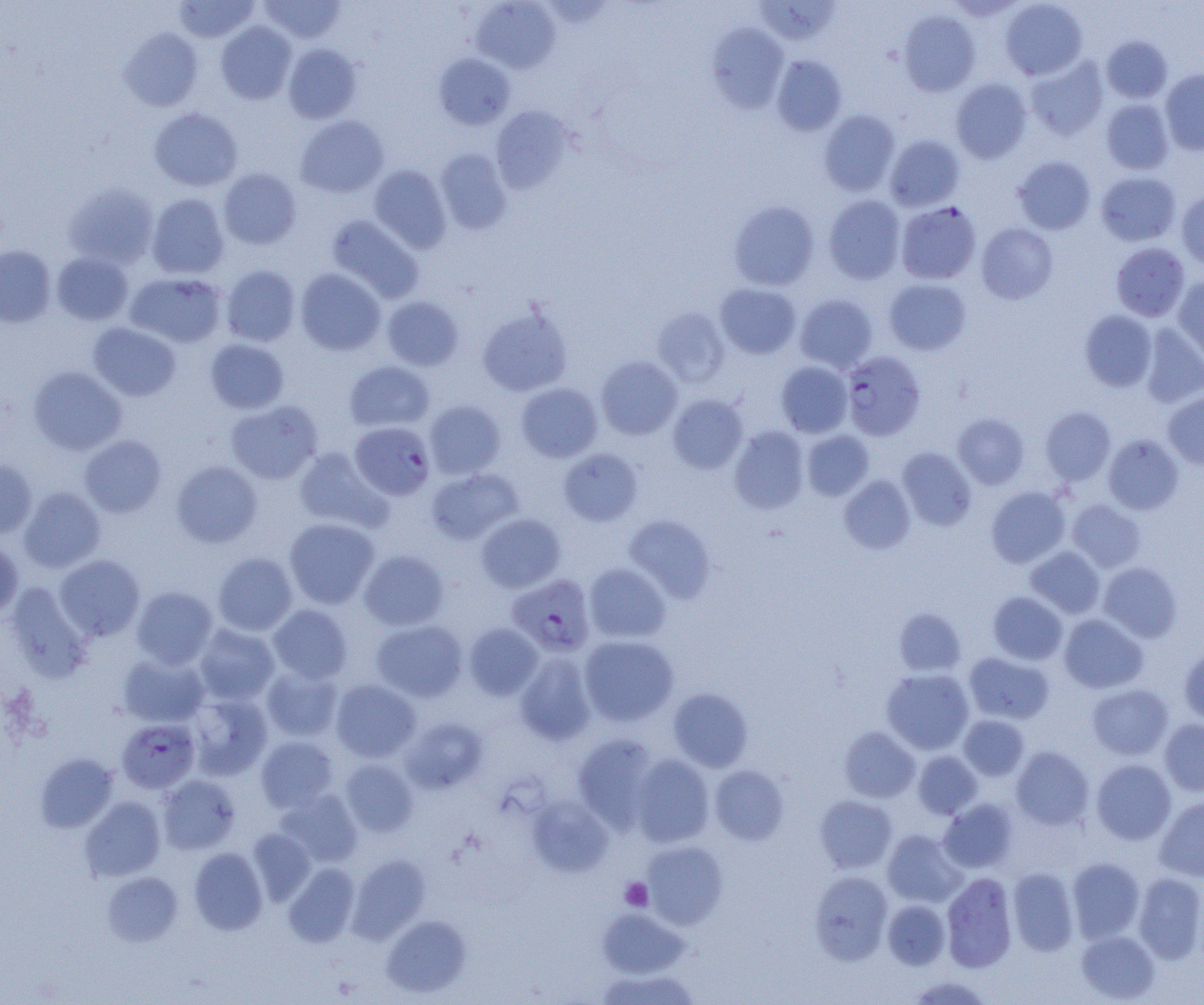
slide-level diagnosis = Plasmodium falciparum
magnification = 1000x
field of view = single
preparation = thin blood film
modality = light microscopy
platelet locations = approximate bounding boxes as [x1, y1, x2, y2] in pixels: [619, 878, 653, 911]
image size = 1204×1005 pixels
Plasmodium falciparum-infected red blood cell locations = approximate bounding boxes as [x1, y1, x2, y2] in pixels: [896, 201, 981, 284], [841, 351, 925, 441], [350, 422, 436, 500], [507, 573, 595, 656], [117, 719, 200, 793]
uninfected red blood cell locations = approximate bounding boxes as [x1, y1, x2, y2] in pixels: [174, 0, 259, 42], [259, 0, 347, 45], [754, 0, 841, 46], [945, 0, 1026, 22], [1000, 0, 1088, 80], [470, 1, 561, 73], [899, 9, 981, 97], [215, 21, 297, 104], [706, 23, 789, 113], [119, 27, 203, 112], [1101, 35, 1173, 103], [283, 44, 361, 124], [433, 52, 516, 130], [771, 55, 847, 136], [1024, 57, 1109, 142], [1159, 68, 1204, 155], [951, 78, 1032, 164], [1101, 98, 1174, 174], [490, 105, 574, 194], [149, 107, 243, 191], [818, 109, 901, 196], [295, 115, 390, 198], [885, 135, 965, 211], [435, 148, 512, 235], [1012, 156, 1096, 235], [368, 165, 452, 253], [218, 168, 302, 250], [1095, 171, 1181, 246], [63, 183, 159, 270], [1177, 191, 1204, 268], [146, 193, 229, 279], [823, 195, 906, 284], [728, 200, 820, 291], [325, 214, 425, 303], [976, 223, 1058, 304], [1110, 242, 1190, 322], [0, 245, 56, 328], [51, 251, 134, 325], [221, 265, 301, 346], [295, 268, 386, 355], [125, 272, 227, 348], [1172, 274, 1204, 367], [883, 278, 971, 355], [715, 283, 801, 359], [795, 293, 878, 373], [382, 296, 463, 370], [477, 303, 574, 396], [651, 307, 730, 387], [1079, 309, 1157, 391], [88, 322, 181, 401], [1139, 323, 1204, 408], [204, 338, 290, 414], [596, 355, 683, 440], [344, 361, 435, 432], [775, 361, 853, 438], [28, 366, 127, 455], [516, 382, 603, 462], [1163, 391, 1204, 471], [668, 393, 748, 474], [225, 400, 323, 485], [424, 400, 505, 479], [1040, 407, 1116, 485], [953, 413, 1030, 489], [729, 426, 809, 513], [802, 430, 874, 501], [1103, 434, 1183, 515], [79, 435, 166, 517], [897, 447, 977, 531], [293, 448, 391, 533], [558, 448, 642, 527], [0, 459, 38, 538], [171, 460, 262, 548], [426, 468, 524, 544], [839, 475, 915, 554], [986, 486, 1071, 567], [19, 487, 106, 572], [1067, 499, 1146, 573], [475, 513, 566, 593], [624, 513, 716, 602], [284, 518, 380, 609], [0, 538, 23, 619], [1025, 546, 1105, 618], [358, 549, 449, 631], [213, 552, 297, 636], [55, 555, 145, 641], [1099, 562, 1183, 642], [584, 563, 670, 644], [5, 583, 92, 681], [131, 586, 217, 669], [987, 591, 1068, 664], [267, 603, 353, 684], [894, 607, 966, 676], [1059, 614, 1148, 693], [371, 619, 467, 701], [464, 623, 543, 700], [193, 624, 280, 704], [579, 635, 679, 726], [1179, 648, 1204, 726], [515, 651, 596, 745], [117, 653, 210, 727], [964, 653, 1054, 724], [261, 665, 344, 741], [882, 668, 974, 754], [331, 679, 421, 762], [1087, 683, 1174, 760], [668, 687, 753, 772], [185, 692, 273, 781], [959, 715, 1029, 781], [400, 717, 487, 794], [1160, 719, 1204, 796], [839, 726, 920, 803], [573, 733, 660, 829], [256, 736, 339, 812], [1011, 747, 1094, 830], [913, 751, 982, 819], [34, 753, 118, 833], [630, 753, 714, 847], [340, 759, 418, 836], [1091, 759, 1176, 845], [709, 764, 789, 845], [156, 774, 241, 854], [274, 789, 363, 867], [814, 795, 898, 873], [80, 796, 165, 881], [528, 797, 614, 876], [1155, 797, 1204, 881], [938, 799, 1018, 873], [247, 828, 315, 905], [882, 830, 967, 907], [641, 841, 728, 929], [188, 847, 268, 935], [348, 855, 430, 944], [1067, 857, 1144, 943], [283, 862, 360, 947], [1008, 868, 1079, 955], [102, 871, 183, 947], [809, 871, 893, 964], [941, 872, 1017, 972], [1133, 872, 1204, 964], [883, 901, 950, 969], [597, 908, 689, 978], [382, 915, 471, 998], [1076, 929, 1159, 1002], [595, 969, 702, 1004], [906, 975, 993, 1005]